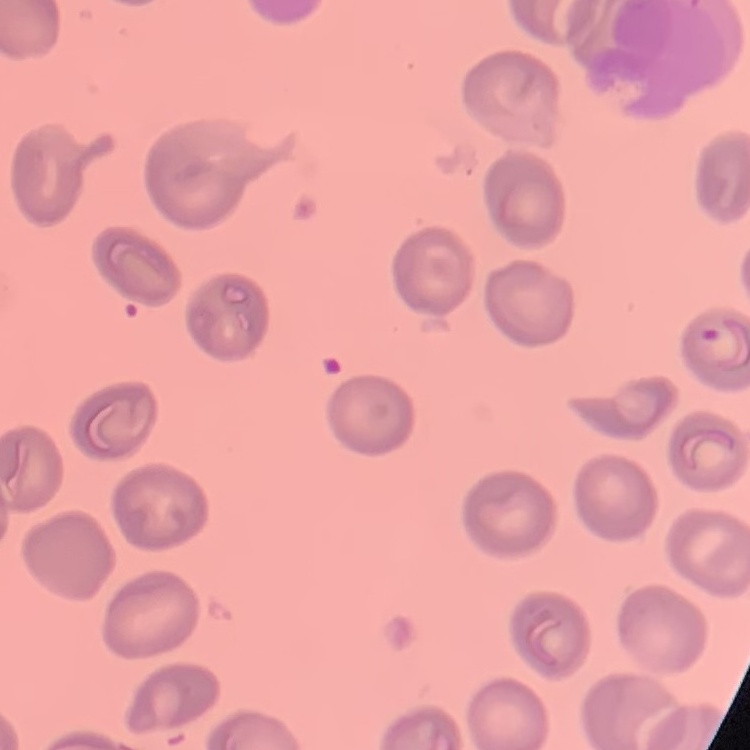
{
  "red_blood_cell_morphology": "no rouleaux formation",
  "image_type": "square crop of a larger photomicrograph",
  "stain": "Field's or Giemsa",
  "preparation": "thin blood smear"
}